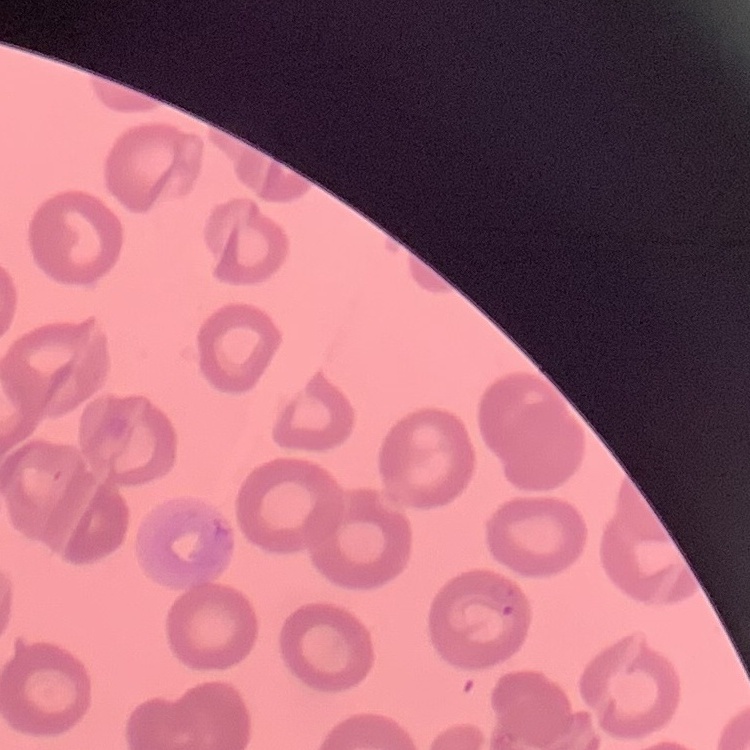

{
  "red_blood_cell_morphology": "no rouleaux formation",
  "stain": "Field's or Giemsa",
  "preparation": "thin blood smear",
  "image_type": "one tile cut from a larger photomicrograph"
}